Report the malaria status of this cell.
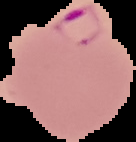

It is parasitized.

From a thin blood smear. The area outside the segmented cell region is set to black. Image is 136×142 pixels.